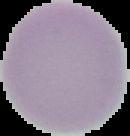
Summary:
  - Image size: 130×136 pixels
  - Image type: segmented cell region on a black background
  - Preparation: thin blood smear
  - Result: no malaria parasites seen